Name the parasite shown.
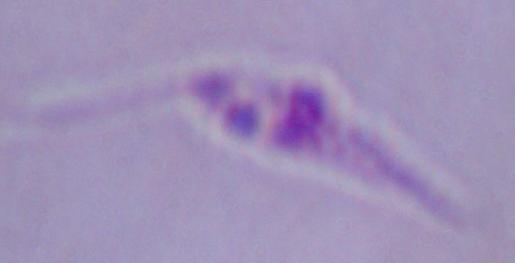
Leishmania.

magnification = 1000x
modality = photomicrograph